Report the malaria status of this cell.
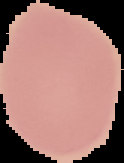
It is uninfected.

Image is 124×163 pixels. From a thin blood smear. The area outside the segmented cell region is set to black.